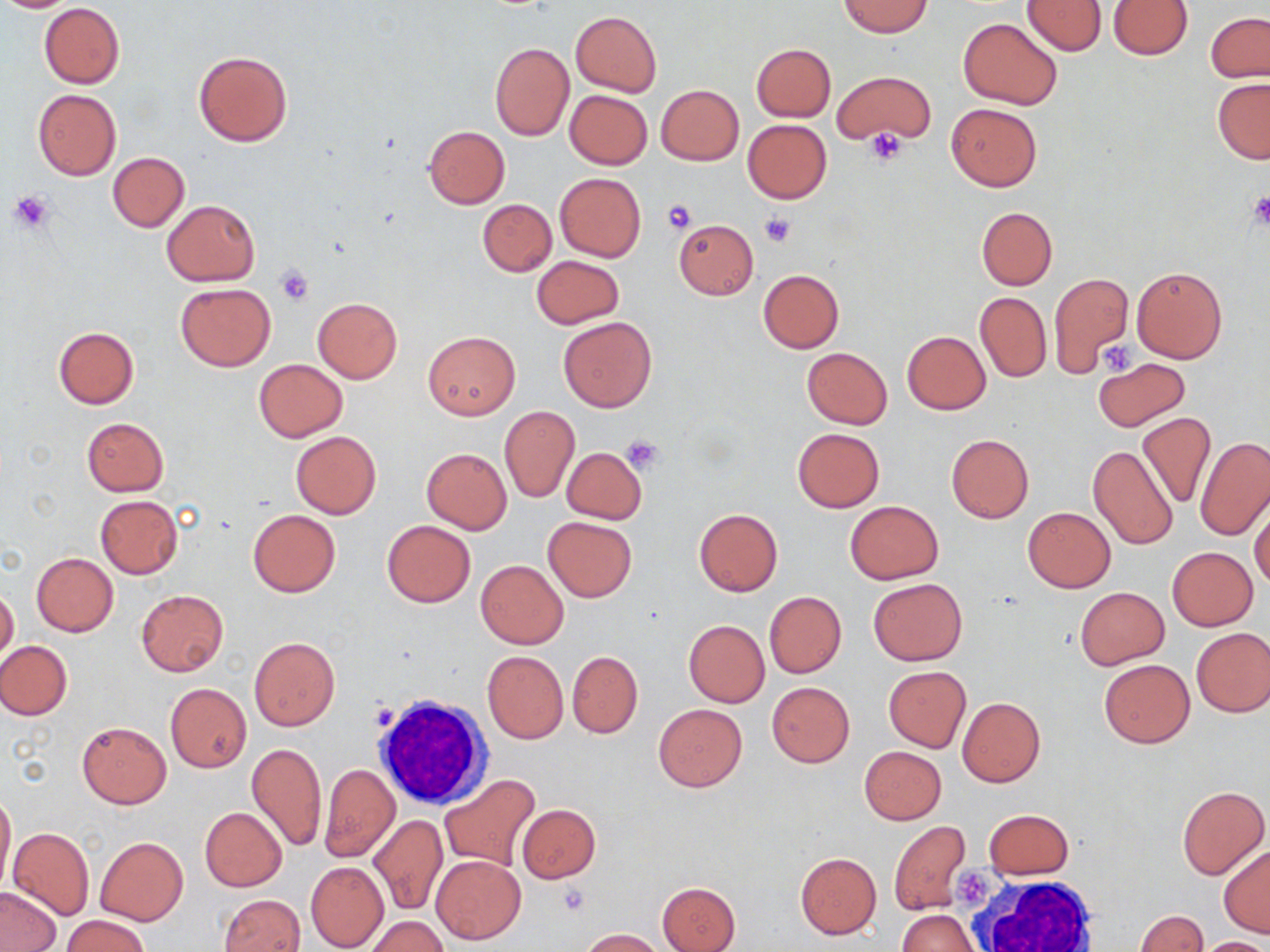
slide-level diagnosis = no evidence of blood parasites
preparation = thin blood smear
platelet locations = approximate bounding boxes as named x1/y1/x2/y2 corners in pixels: (x1=866, y1=129, x2=908, y2=164), (x1=8, y1=191, x2=54, y2=234), (x1=1245, y1=192, x2=1270, y2=230), (x1=660, y1=200, x2=697, y2=234), (x1=758, y1=214, x2=795, y2=247), (x1=274, y1=265, x2=314, y2=306), (x1=1099, y1=342, x2=1137, y2=376), (x1=622, y1=436, x2=665, y2=473), (x1=370, y1=703, x2=398, y2=733), (x1=956, y1=865, x2=997, y2=912), (x1=557, y1=884, x2=592, y2=916)
magnification = 1000x
white blood cell locations = approximate bounding boxes as named x1/y1/x2/y2 corners in pixels: (x1=376, y1=693, x2=489, y2=806), (x1=962, y1=873, x2=1101, y2=952)
stain = May-Grünwald-Giemsa
field of view = one of a larger specimen
uninfected red blood cell locations = approximate bounding boxes as named x1/y1/x2/y2 corners in pixels: (x1=0, y1=0, x2=81, y2=13), (x1=1022, y1=1, x2=1107, y2=55), (x1=1107, y1=1, x2=1192, y2=59), (x1=838, y1=2, x2=933, y2=37), (x1=39, y1=3, x2=125, y2=88), (x1=570, y1=10, x2=661, y2=98), (x1=1206, y1=12, x2=1270, y2=82), (x1=959, y1=18, x2=1062, y2=109), (x1=490, y1=43, x2=573, y2=141), (x1=751, y1=43, x2=835, y2=121), (x1=194, y1=50, x2=292, y2=147), (x1=833, y1=70, x2=935, y2=146), (x1=1213, y1=78, x2=1270, y2=163), (x1=656, y1=84, x2=743, y2=165), (x1=32, y1=89, x2=120, y2=181), (x1=564, y1=90, x2=651, y2=170), (x1=947, y1=102, x2=1043, y2=190), (x1=742, y1=119, x2=832, y2=204), (x1=422, y1=126, x2=510, y2=207), (x1=108, y1=152, x2=189, y2=231), (x1=553, y1=172, x2=646, y2=262), (x1=478, y1=199, x2=556, y2=277), (x1=162, y1=200, x2=260, y2=286), (x1=976, y1=207, x2=1057, y2=290), (x1=673, y1=219, x2=758, y2=299), (x1=532, y1=255, x2=623, y2=329), (x1=1131, y1=266, x2=1227, y2=363), (x1=757, y1=269, x2=844, y2=353), (x1=1048, y1=271, x2=1133, y2=376), (x1=175, y1=283, x2=275, y2=372), (x1=975, y1=292, x2=1051, y2=383), (x1=313, y1=297, x2=402, y2=383), (x1=558, y1=316, x2=656, y2=412), (x1=53, y1=326, x2=138, y2=408), (x1=902, y1=330, x2=990, y2=415), (x1=423, y1=331, x2=520, y2=419), (x1=801, y1=347, x2=892, y2=428), (x1=253, y1=358, x2=348, y2=442), (x1=1094, y1=358, x2=1190, y2=432), (x1=499, y1=405, x2=579, y2=503), (x1=1137, y1=412, x2=1213, y2=508), (x1=83, y1=417, x2=168, y2=495), (x1=792, y1=428, x2=884, y2=513), (x1=291, y1=431, x2=381, y2=519), (x1=946, y1=434, x2=1033, y2=523), (x1=1195, y1=436, x2=1270, y2=540), (x1=1087, y1=444, x2=1179, y2=550), (x1=421, y1=447, x2=511, y2=534), (x1=562, y1=448, x2=647, y2=525), (x1=1250, y1=495, x2=1270, y2=590), (x1=95, y1=496, x2=183, y2=578), (x1=845, y1=501, x2=943, y2=584), (x1=1022, y1=507, x2=1116, y2=593), (x1=693, y1=509, x2=783, y2=596), (x1=247, y1=510, x2=341, y2=596), (x1=543, y1=516, x2=636, y2=601), (x1=381, y1=520, x2=476, y2=608), (x1=1166, y1=547, x2=1258, y2=631), (x1=32, y1=553, x2=118, y2=637), (x1=476, y1=560, x2=568, y2=648), (x1=868, y1=578, x2=966, y2=665), (x1=1, y1=586, x2=19, y2=663), (x1=1076, y1=588, x2=1168, y2=668), (x1=136, y1=589, x2=229, y2=676), (x1=764, y1=592, x2=846, y2=677), (x1=683, y1=620, x2=769, y2=707), (x1=1192, y1=627, x2=1270, y2=717), (x1=249, y1=636, x2=339, y2=731), (x1=0, y1=640, x2=72, y2=719), (x1=482, y1=651, x2=569, y2=743), (x1=567, y1=651, x2=643, y2=738), (x1=1099, y1=658, x2=1194, y2=748), (x1=883, y1=665, x2=970, y2=752), (x1=767, y1=681, x2=855, y2=767), (x1=165, y1=684, x2=252, y2=772), (x1=958, y1=697, x2=1045, y2=787), (x1=653, y1=704, x2=746, y2=791), (x1=77, y1=722, x2=171, y2=808), (x1=247, y1=743, x2=326, y2=852), (x1=859, y1=746, x2=946, y2=824), (x1=319, y1=764, x2=399, y2=861), (x1=440, y1=774, x2=541, y2=869), (x1=1176, y1=784, x2=1269, y2=880), (x1=0, y1=787, x2=15, y2=893), (x1=518, y1=804, x2=600, y2=883), (x1=199, y1=807, x2=286, y2=892), (x1=984, y1=809, x2=1073, y2=879), (x1=368, y1=815, x2=447, y2=915), (x1=889, y1=821, x2=971, y2=915), (x1=8, y1=826, x2=95, y2=921), (x1=95, y1=837, x2=187, y2=926), (x1=1219, y1=845, x2=1270, y2=937), (x1=795, y1=852, x2=880, y2=939), (x1=433, y1=856, x2=526, y2=944), (x1=306, y1=863, x2=388, y2=950), (x1=657, y1=881, x2=741, y2=952), (x1=1, y1=888, x2=60, y2=951), (x1=218, y1=894, x2=304, y2=952), (x1=897, y1=910, x2=980, y2=952), (x1=1136, y1=910, x2=1207, y2=952), (x1=60, y1=915, x2=150, y2=952), (x1=366, y1=916, x2=448, y2=952), (x1=579, y1=928, x2=667, y2=951), (x1=1197, y1=937, x2=1269, y2=952)
modality = light microscopy
image size = 1270×952 pixels